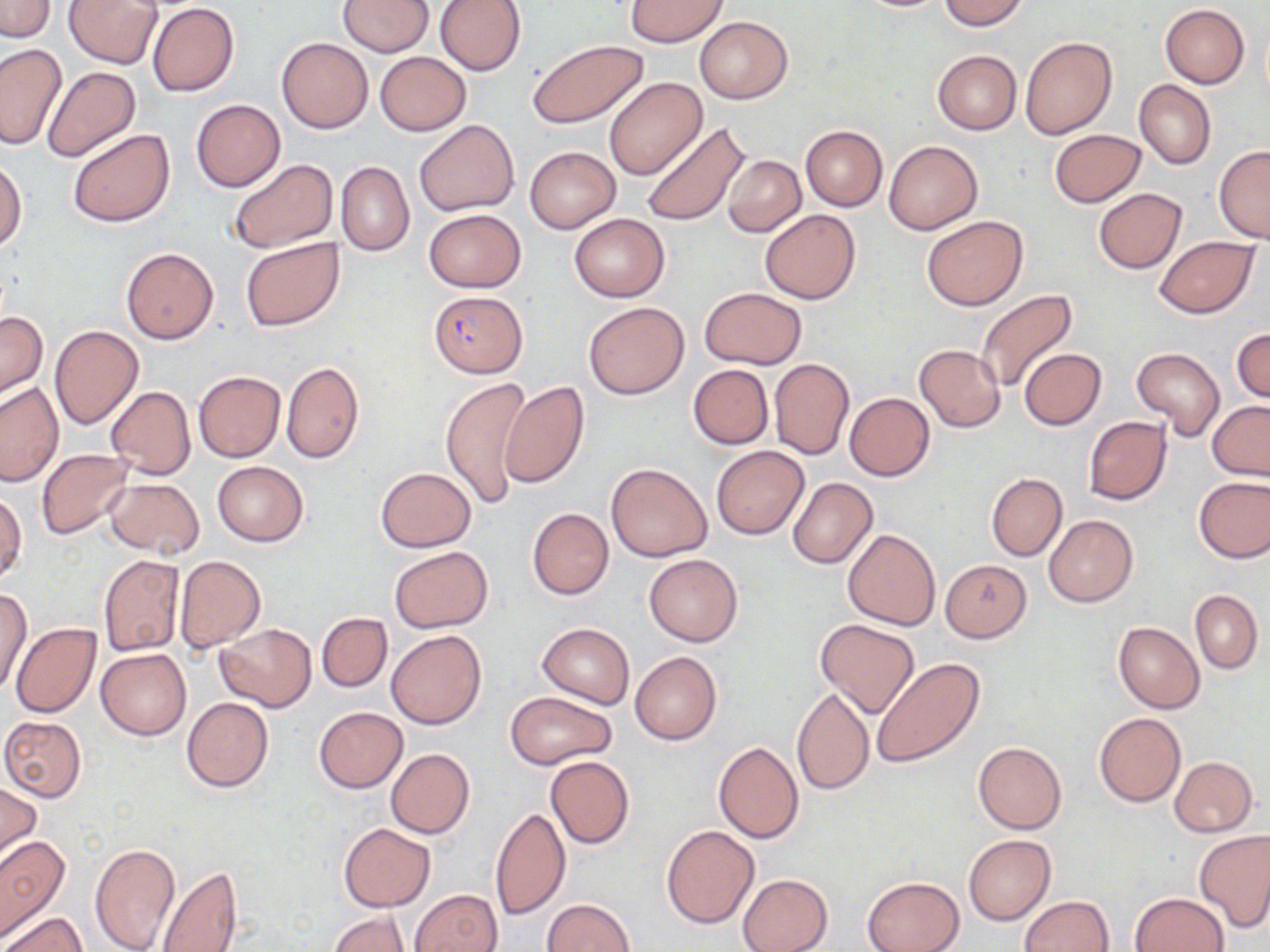
slide_level_diagnosis: Plasmodium falciparum
stain: May-Grünwald-Giemsa
magnification: 1000x
field_of_view: single
image_size: 1270×952 pixels
plasmodium_falciparum_infected_red_blood_cell_locations: 'approximate bounding boxes as (x1,y1)-(x2,y2) corner pairs in pixels: (429,291)-(527,378)'
preparation: thin blood film
uninfected_red_blood_cell_locations: 'approximate bounding boxes as (x1,y1)-(x2,y2) corner pairs in pixels: (64,0)-(164,67), (338,0)-(435,56), (435,0)-(526,75), (624,0)-(729,47), (849,0)-(952,12), (939,0)-(1029,31), (0,1)-(55,40), (147,3)-(239,96), (1160,4)-(1249,87), (694,16)-(792,104), (276,37)-(373,132), (1020,37)-(1117,140), (527,39)-(649,128), (0,44)-(65,150), (931,49)-(1022,134), (374,52)-(469,135), (41,66)-(139,163), (604,77)-(707,179), (1133,79)-(1216,169), (191,99)-(285,191), (414,120)-(519,217), (641,120)-(751,227), (800,125)-(888,211), (68,129)-(175,228), (1048,129)-(1146,207), (884,141)-(982,234), (1214,145)-(1270,244), (524,146)-(620,232), (724,155)-(805,236), (0,156)-(26,253), (226,158)-(337,255), (336,162)-(414,256), (1093,188)-(1188,273), (423,209)-(525,292), (760,209)-(860,303), (569,214)-(669,301), (921,215)-(1028,311), (1153,236)-(1258,319), (240,237)-(345,332), (120,246)-(219,345), (699,287)-(807,370), (976,289)-(1079,393), (583,302)-(688,399), (0,311)-(47,399), (48,325)-(144,430), (1232,325)-(1270,404), (913,343)-(1005,431), (1132,347)-(1225,441), (1018,348)-(1106,431), (769,357)-(854,459), (280,361)-(364,464), (687,364)-(774,450), (193,370)-(285,462), (439,376)-(534,509), (499,381)-(591,489), (0,382)-(65,485), (106,386)-(196,480), (844,392)-(935,482), (1206,401)-(1270,479), (1083,416)-(1172,505), (711,446)-(808,539), (37,450)-(135,540), (212,461)-(307,546), (607,462)-(713,562), (376,467)-(476,551), (986,472)-(1067,560), (1194,475)-(1270,563), (104,478)-(204,558), (786,478)-(877,569), (0,490)-(26,583), (527,508)-(614,599), (1044,514)-(1137,607), (843,528)-(941,631), (388,546)-(493,633), (99,554)-(184,655), (644,554)-(743,646), (174,555)-(266,653), (939,557)-(1032,642), (0,586)-(32,698), (1190,591)-(1262,673), (317,612)-(391,692), (814,619)-(920,721), (1113,621)-(1205,713), (216,623)-(316,711), (537,623)-(634,707), (11,624)-(102,719), (386,629)-(487,729), (96,649)-(191,740), (630,651)-(721,745), (873,657)-(984,768), (792,686)-(875,797), (505,691)-(618,770), (181,697)-(272,792), (314,707)-(407,792), (1093,712)-(1186,806), (0,717)-(86,801), (713,741)-(803,844), (973,742)-(1067,834), (386,748)-(474,838), (545,755)-(635,849), (1169,756)-(1257,837), (0,781)-(42,867), (490,808)-(570,919), (338,822)-(436,912), (660,825)-(759,929), (1194,830)-(1270,932), (963,834)-(1055,925), (0,835)-(70,942), (90,843)-(179,952), (154,865)-(240,952), (738,873)-(833,952), (862,876)-(964,952), (410,889)-(502,952), (1129,892)-(1229,952), (1020,895)-(1114,952), (541,899)-(635,952), (327,911)-(408,952), (3,913)-(86,952)'
modality: optical microscopy